Describe the morphology of the red blood cells.
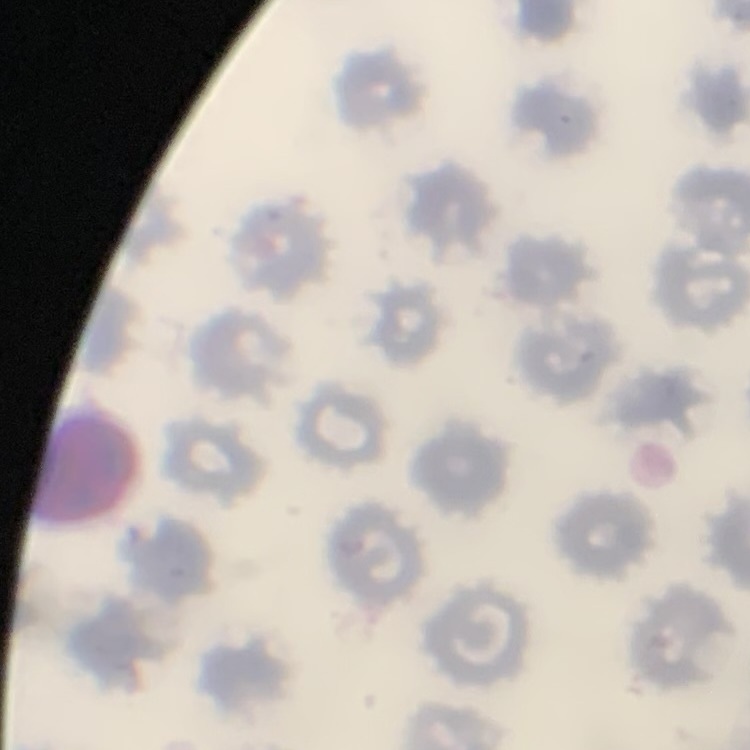

They show no rouleaux formation.

Summary:
  - Stain: Field's or Giemsa
  - Preparation: thin peripheral smear
  - Image type: square crop of a larger photomicrograph